Assess this cell for malaria.
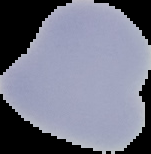
Uninfected.

image type = segmented cell region on a black background
preparation = thin blood smear
image size = 151×154 pixels